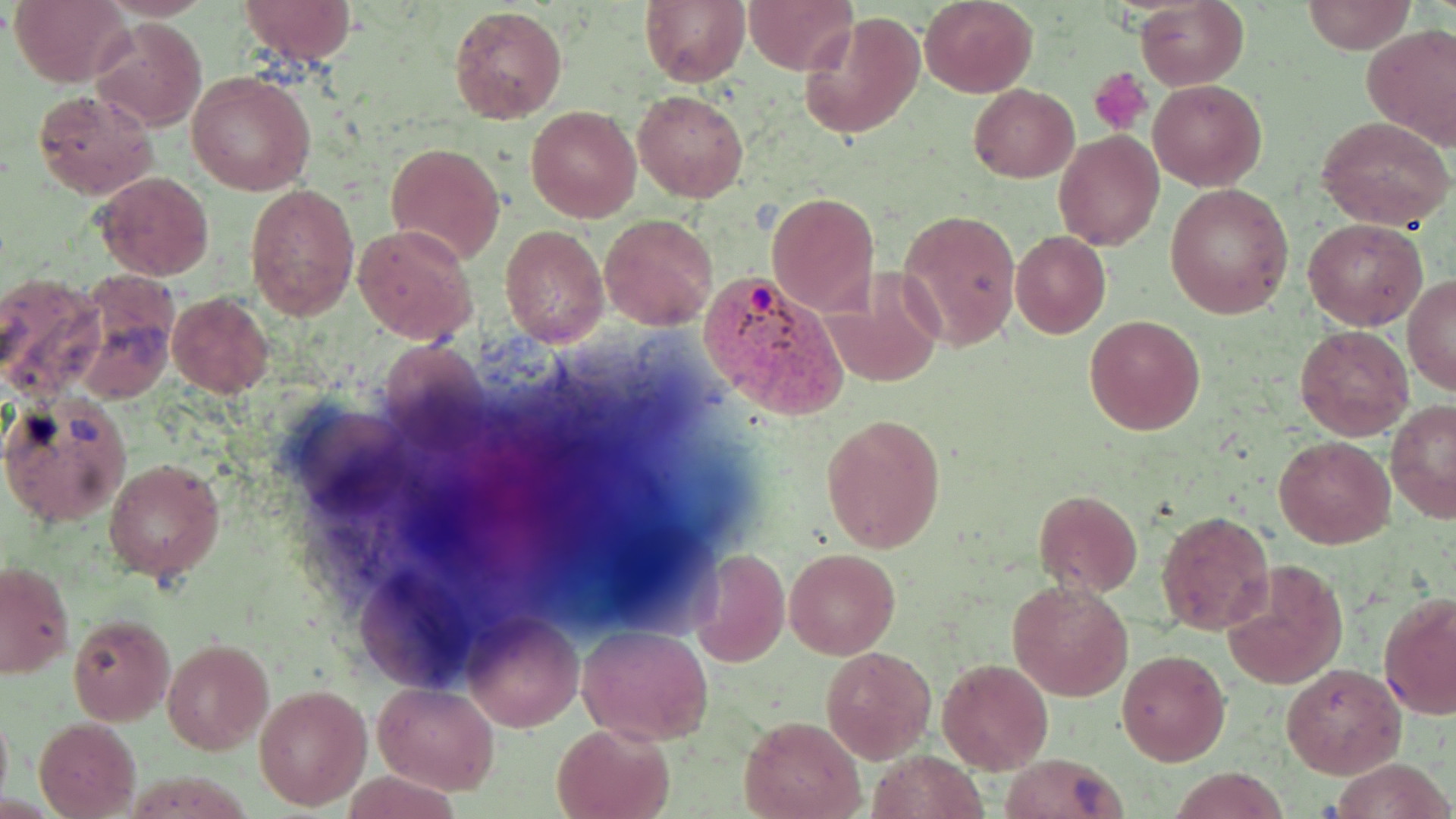
Summary:
  - Coordinate format: approximate bounding boxes as (x1,y1)-(x2,y2) corner pairs in pixels
  - Platelet locations: (1089,67)-(1150,135)
  - Uninfected red blood cell locations: (10,0)-(132,87), (239,0)-(359,67), (640,0)-(750,86), (743,0)-(857,73), (919,0)-(1038,98), (1136,0)-(1249,90), (1303,0)-(1414,54), (448,4)-(568,122), (799,13)-(925,141), (92,20)-(207,131), (1361,22)-(1456,152), (185,69)-(316,195), (1148,79)-(1266,190), (969,83)-(1078,182), (33,88)-(156,198), (633,90)-(750,203), (527,105)-(640,222), (1317,117)-(1454,231), (1054,132)-(1164,251), (386,141)-(505,266), (95,172)-(216,280), (244,182)-(359,320), (1163,183)-(1294,318), (768,192)-(879,316), (898,209)-(1020,349), (600,213)-(717,330), (1305,217)-(1428,330), (354,225)-(477,344), (500,225)-(608,346), (1010,231)-(1110,338), (820,268)-(949,390), (0,272)-(105,399), (1403,275)-(1456,397), (168,292)-(276,398), (1085,314)-(1205,435), (1294,324)-(1416,441), (0,394)-(133,528), (1386,400)-(1456,523), (821,414)-(947,553), (1273,434)-(1395,549), (104,458)-(225,581), (1032,489)-(1142,596), (1154,509)-(1274,636), (689,548)-(789,667), (785,548)-(899,659), (1221,558)-(1348,690), (1,561)-(74,678), (1007,578)-(1133,701), (1380,592)-(1456,720), (462,612)-(583,734), (68,615)-(174,726), (575,625)-(714,745), (162,638)-(275,755), (822,646)-(935,763), (1116,648)-(1231,765), (937,659)-(1052,772), (1279,664)-(1404,779), (375,683)-(500,795), (255,684)-(372,810), (0,706)-(12,810), (740,716)-(865,819), (33,718)-(141,818), (551,722)-(674,819), (868,749)-(987,819), (999,754)-(1127,819), (1331,757)-(1456,818), (1166,767)-(1287,819), (343,768)-(468,818)
  - Plasmodium vivax-infected red blood cell locations: (697,267)-(850,419)
  - Slide-level diagnosis: Plasmodium vivax
  - Image size: 1456×819 pixels
  - Preparation: thin blood film
  - Magnification: 1000x
  - Stain: May-Grünwald-Giemsa
  - Field of view: single
  - Modality: light microscopy